Locate platelets.
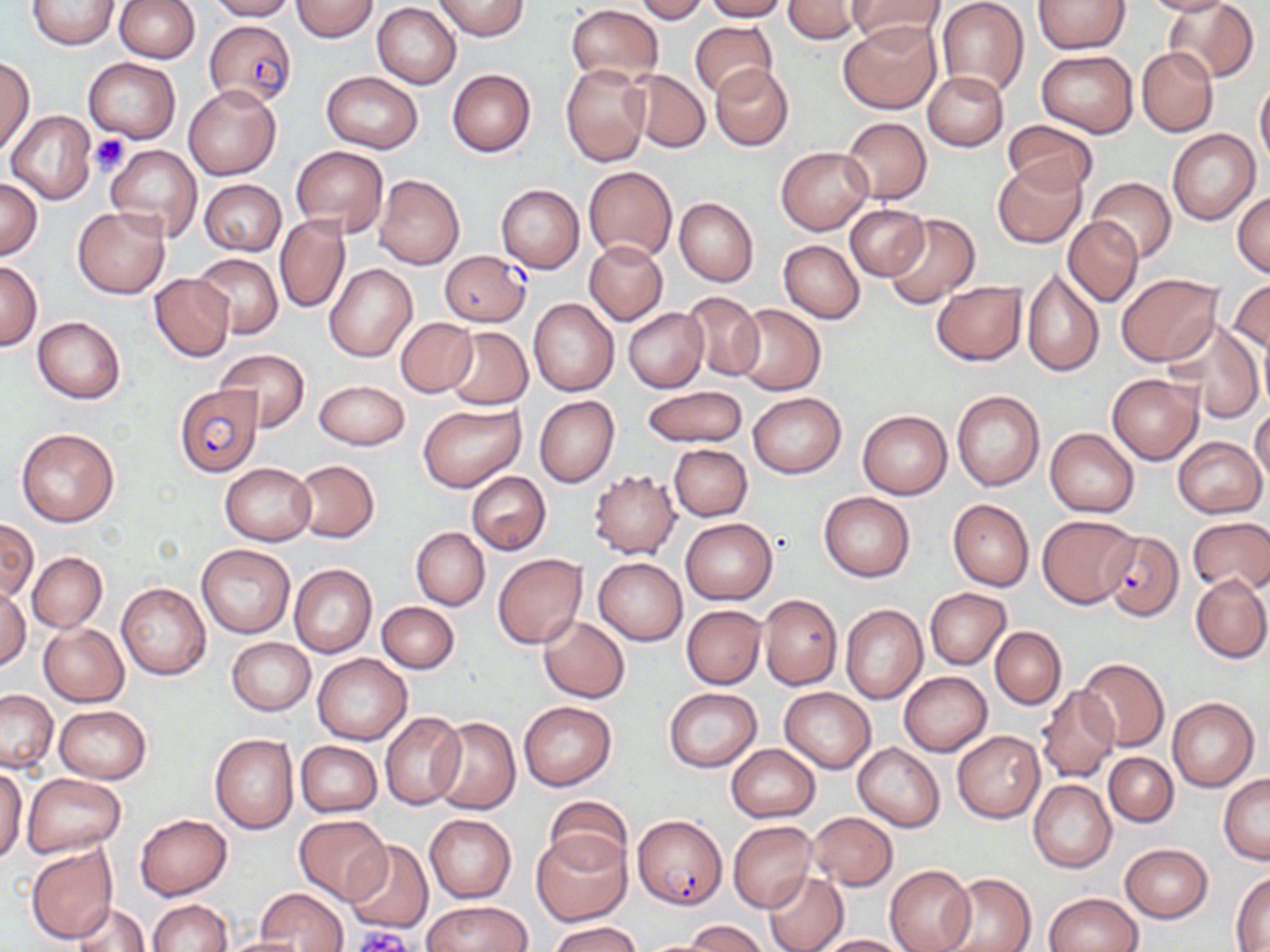
Approximate bounding boxes as (x1, y1, x2, y2) in pixels.
Platelets: (89, 133, 130, 175), (351, 926, 410, 950).

slide-level diagnosis = Plasmodium falciparum
stain = May-Grünwald-Giemsa
magnification = 1000x
field of view = one of a larger specimen
image size = 1270×952 pixels
Plasmodium falciparum-infected red blood cell locations = approximate bounding boxes as (x1, y1, x2, y2) in pixels: (204, 20, 296, 108), (440, 251, 530, 327), (173, 385, 261, 477), (1103, 530, 1184, 621), (633, 814, 727, 910)
modality = optical microscopy
preparation = thin blood film
uninfected red blood cell locations = approximate bounding boxes as (x1, y1, x2, y2) in pixels: (115, 0, 199, 62), (207, 0, 294, 20), (292, 0, 379, 42), (634, 0, 709, 23), (705, 0, 787, 21), (783, 0, 863, 44), (848, 0, 945, 45), (935, 0, 1029, 98), (1140, 0, 1235, 15), (1166, 0, 1258, 84), (28, 1, 120, 50), (433, 1, 529, 40), (1032, 1, 1130, 53), (373, 3, 461, 87), (566, 4, 663, 86), (691, 20, 776, 101), (840, 20, 940, 113), (1136, 47, 1218, 137), (1035, 50, 1138, 136), (83, 57, 181, 144), (1, 58, 34, 153), (560, 62, 651, 166), (710, 64, 794, 151), (447, 68, 536, 157), (626, 69, 709, 153), (923, 70, 1009, 152), (321, 72, 422, 154), (1255, 77, 1270, 171), (182, 82, 282, 180), (7, 111, 97, 204), (840, 116, 932, 204), (1001, 120, 1101, 197), (1167, 129, 1259, 225), (106, 145, 202, 242), (292, 147, 389, 237), (776, 147, 872, 234), (992, 160, 1086, 248), (583, 166, 677, 261), (373, 174, 465, 270), (1086, 176, 1176, 263), (0, 177, 43, 258), (199, 179, 286, 256), (496, 184, 584, 273), (1232, 191, 1270, 277), (675, 197, 758, 288), (845, 204, 929, 281), (73, 207, 169, 298), (275, 213, 351, 314), (883, 213, 979, 310), (1063, 217, 1143, 306), (778, 240, 865, 323), (584, 242, 667, 325), (194, 253, 282, 339), (0, 261, 43, 350), (325, 265, 417, 363), (1022, 267, 1104, 378), (149, 273, 233, 361), (1116, 274, 1223, 366), (1229, 278, 1270, 355), (931, 280, 1027, 365), (680, 292, 765, 383), (529, 298, 619, 396), (731, 303, 825, 395), (623, 307, 708, 393), (32, 316, 126, 404), (394, 317, 477, 397), (1163, 320, 1265, 423), (445, 327, 532, 410), (215, 349, 310, 430), (1106, 372, 1202, 464), (315, 379, 408, 449), (641, 385, 747, 448), (951, 391, 1044, 491), (747, 392, 846, 478), (534, 396, 619, 487), (418, 402, 525, 492), (1250, 406, 1270, 487), (858, 410, 952, 499), (16, 427, 120, 527), (1044, 427, 1138, 517), (1172, 436, 1266, 518), (668, 443, 752, 521), (293, 461, 379, 543), (220, 462, 316, 546), (588, 469, 680, 558), (467, 470, 551, 555), (818, 492, 915, 581), (947, 499, 1034, 591), (1036, 514, 1139, 608), (1187, 516, 1270, 593), (680, 518, 777, 604), (0, 519, 38, 601), (411, 527, 489, 610), (197, 545, 295, 638), (27, 552, 107, 632), (492, 554, 587, 648), (593, 557, 686, 645), (289, 563, 378, 658), (1191, 573, 1270, 664), (116, 582, 211, 680), (0, 586, 30, 669), (924, 588, 1012, 669), (759, 593, 842, 690), (376, 602, 459, 674), (840, 604, 928, 704), (682, 605, 766, 689), (538, 616, 629, 704), (39, 622, 129, 706), (990, 626, 1066, 708), (227, 637, 315, 716), (314, 653, 411, 744), (1077, 657, 1168, 752), (898, 671, 992, 756), (1036, 685, 1120, 784), (779, 687, 874, 773), (663, 688, 762, 771), (0, 690, 58, 772), (1167, 697, 1258, 792), (519, 701, 617, 791), (53, 705, 151, 783), (380, 712, 464, 809), (430, 717, 520, 815), (952, 730, 1044, 822), (210, 733, 298, 834), (295, 741, 381, 817), (853, 742, 944, 831), (725, 743, 820, 822), (1104, 752, 1177, 826), (0, 767, 27, 863), (22, 773, 124, 857), (1218, 774, 1270, 864), (1029, 780, 1116, 873), (546, 794, 630, 873), (806, 812, 899, 891), (136, 814, 232, 899), (293, 814, 391, 904), (424, 814, 516, 904), (727, 820, 816, 913), (531, 829, 631, 926), (345, 840, 433, 932), (1119, 843, 1214, 923), (25, 845, 118, 944), (885, 865, 975, 952), (763, 870, 848, 952), (1230, 872, 1270, 950), (939, 873, 1035, 952), (258, 888, 346, 951), (1045, 891, 1143, 952), (146, 899, 232, 952), (423, 901, 528, 951), (71, 903, 150, 952), (685, 920, 768, 952), (549, 921, 643, 952), (816, 934, 911, 952), (220, 936, 312, 952)